Describe the morphology of the erythrocytes.
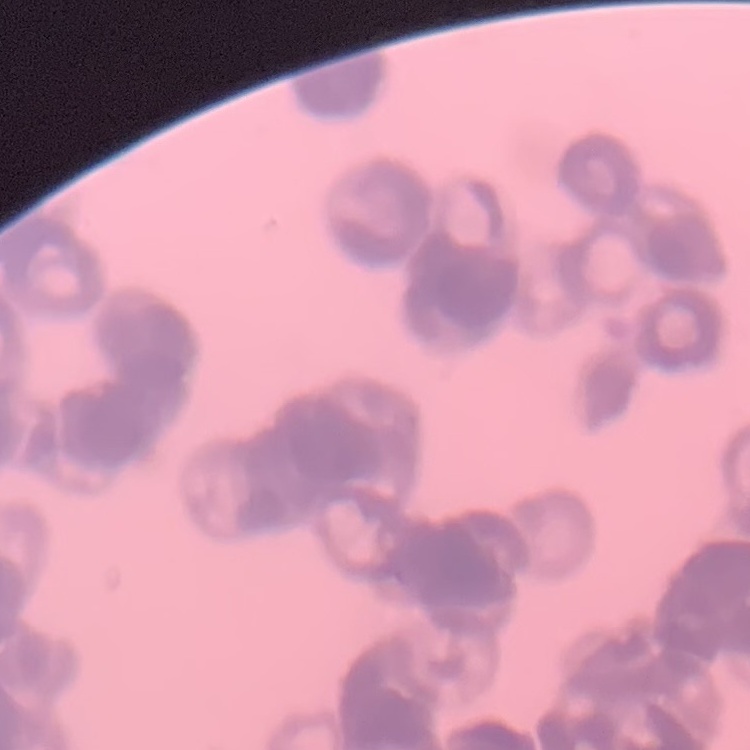

They show rouleaux formation.

Summary:
  - Preparation: thin peripheral smear
  - Stain: Field's or Giemsa
  - Image type: square crop of a larger photomicrograph